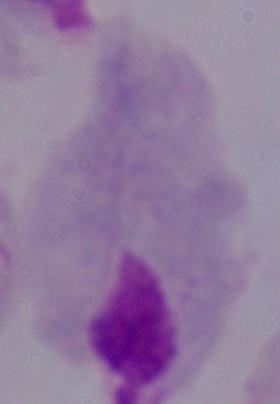
1000x magnification. A trichomonad is seen. Micrograph.